Assess this cell for malaria.
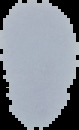
Uninfected.

Summary:
  - Image type: segmented cell region on a black background
  - Image size: 79×130 pixels
  - Preparation: thin blood smear